Assess the morphology of the erythrocytes.
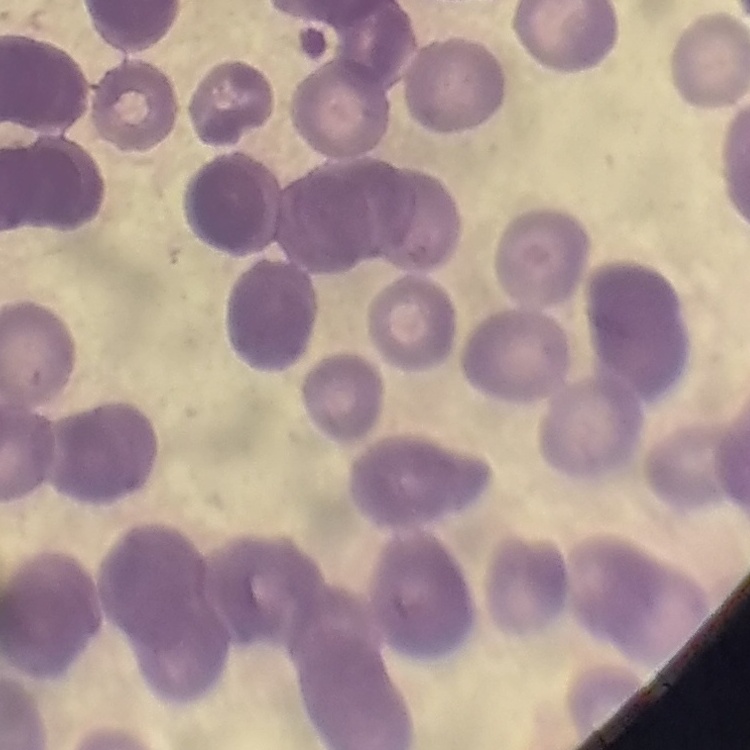

Rouleaux formation.

{
  "preparation": "thin blood film",
  "stain": "Field's or Giemsa",
  "image_type": "one tile cut from a larger photomicrograph"
}